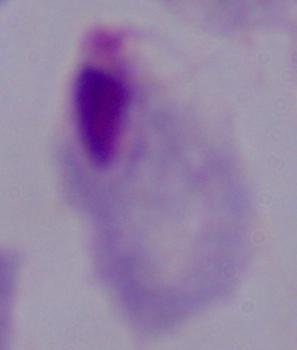
Summary:
  - Identification: trichomonad
  - Magnification: 1000x
  - Modality: photomicrograph